Assess this cell for malaria.
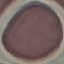
Uninfected.

Giemsa stain. Acquired by smartphone through the microscope eyepiece. Cell patch, automatically extracted from a larger field of view and resized to 64 × 64 pixels. Thin blood film.